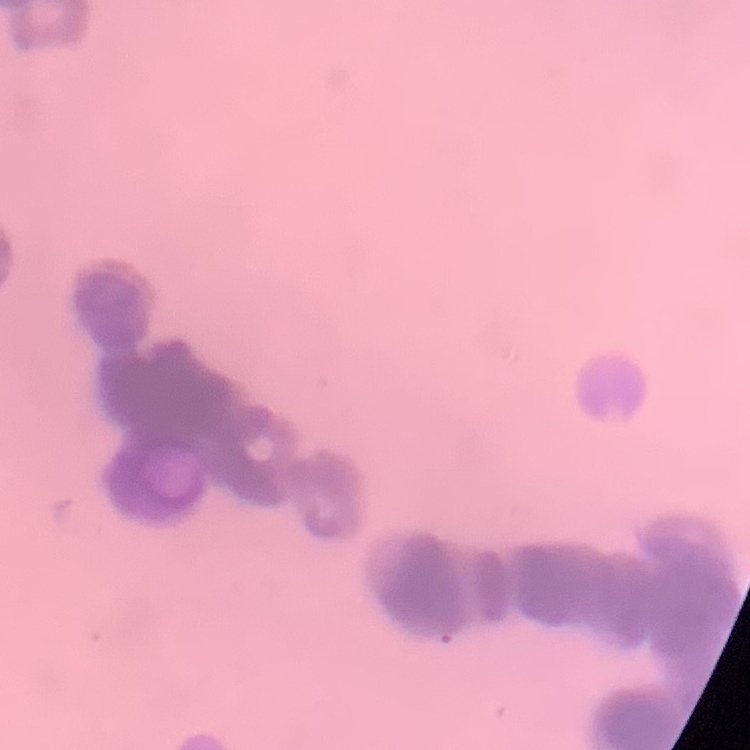
red_blood_cell_morphology: rouleaux formation
stain: Field's or Giemsa
image_type: one tile cut from a larger photomicrograph
preparation: thin blood smear